Assess this cell for malaria.
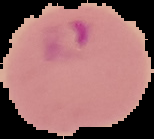
It is parasitized.

From a thin blood smear. Cell region segmented out of the field of view; the surrounding area is masked to black. Image is 154×139 pixels.